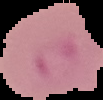

Segmented cell region on a black background. Image is 103×100 pixels. Result: malaria parasites detected. From a thin blood smear.